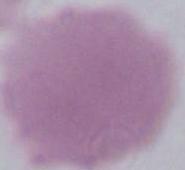

Summary:
  - Modality: micrograph
  - Identification: red blood cell
  - Magnification: 1000x